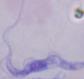

{
  "modality": "micrograph",
  "identification": "trypanosome",
  "magnification": "1000x"
}